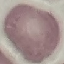

Summary:
  - Malaria status: uninfected
  - Stain: Giemsa
  - Preparation: thin smear
  - Capture: smartphone camera at the microscope eyepiece
  - Image type: automatically extracted cell patch, resized to 64 × 64 pixels